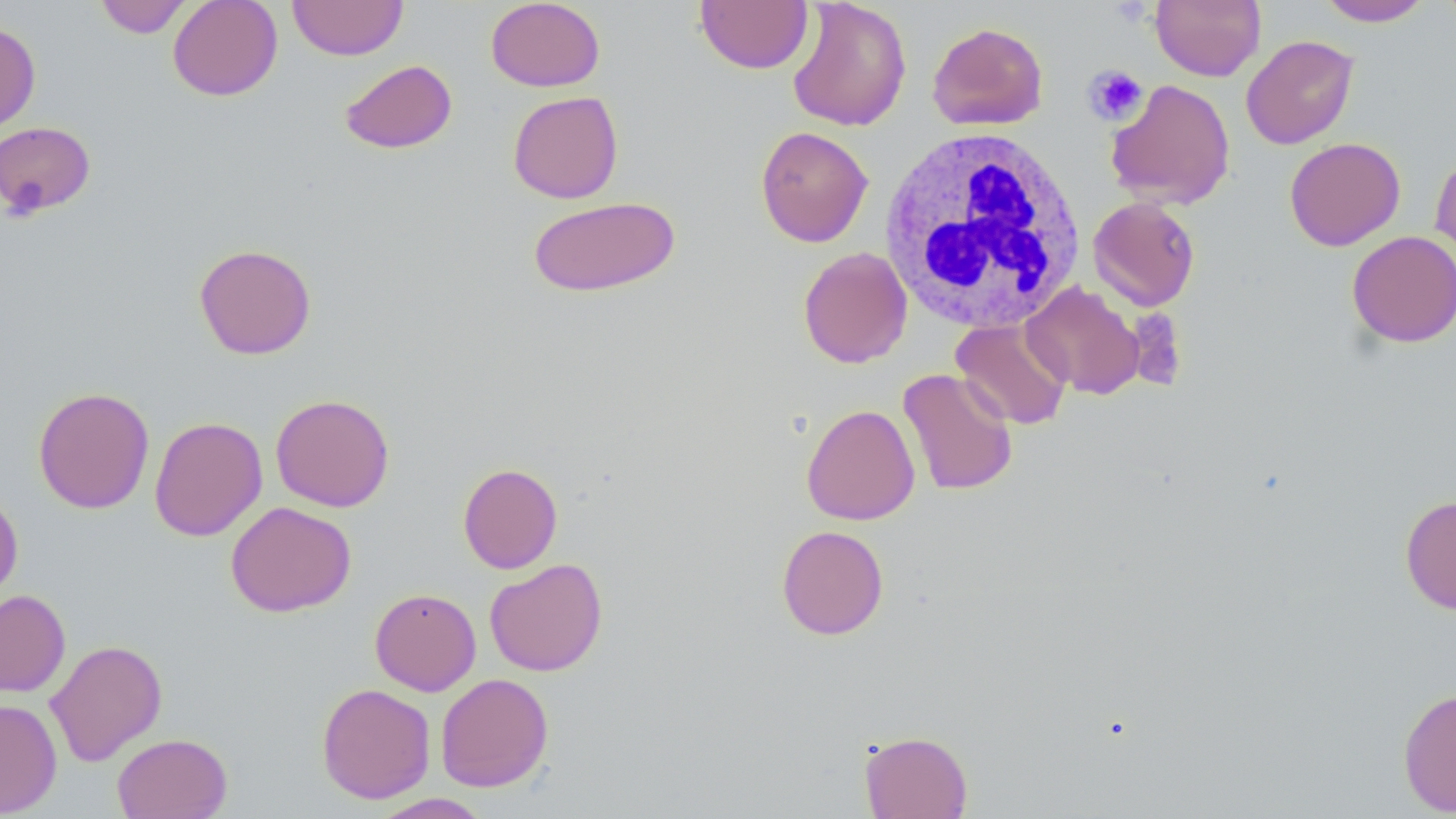
slide-level diagnosis = no evidence of blood parasites
stain = May-Grünwald-Giemsa
platelet locations = approximate bounding boxes as (x1, y1, x2, y2) in pixels: (1083, 64, 1149, 126)
preparation = thin blood film
field of view = one of a larger specimen
white blood cell locations = approximate bounding boxes as (x1, y1, x2, y2) in pixels: (879, 126, 1087, 332)
image size = 1456×819 pixels
modality = optical microscopy
magnification = 1000x
uninfected red blood cell locations = approximate bounding boxes as (x1, y1, x2, y2) in pixels: (93, 0, 194, 38), (167, 0, 283, 101), (287, 0, 409, 60), (486, 0, 605, 92), (787, 0, 912, 132), (1150, 0, 1266, 81), (1317, 0, 1434, 26), (695, 1, 812, 74), (1439, 1, 1456, 34), (0, 22, 41, 134), (927, 22, 1049, 131), (1241, 34, 1359, 150), (339, 59, 458, 154), (1105, 78, 1236, 210), (507, 91, 624, 204), (0, 121, 96, 220), (755, 125, 873, 248), (1284, 137, 1405, 251), (1430, 150, 1456, 275), (526, 195, 681, 298), (1088, 197, 1200, 311), (1346, 230, 1456, 348), (194, 243, 317, 360), (797, 246, 912, 368), (1022, 281, 1145, 399), (951, 318, 1072, 430), (898, 368, 1018, 496), (33, 386, 155, 514), (270, 393, 395, 512), (801, 404, 920, 525), (149, 416, 268, 542), (457, 463, 563, 574), (0, 489, 23, 604), (1400, 495, 1456, 615), (226, 501, 356, 617), (776, 524, 889, 640), (484, 558, 608, 677), (370, 588, 481, 695), (0, 589, 71, 697), (45, 639, 167, 766), (435, 673, 554, 792), (316, 683, 436, 804), (1397, 687, 1456, 816), (0, 698, 62, 817), (859, 730, 973, 818), (112, 733, 232, 819), (369, 793, 493, 818)